Locate every malaria parasite and every leukocyte.
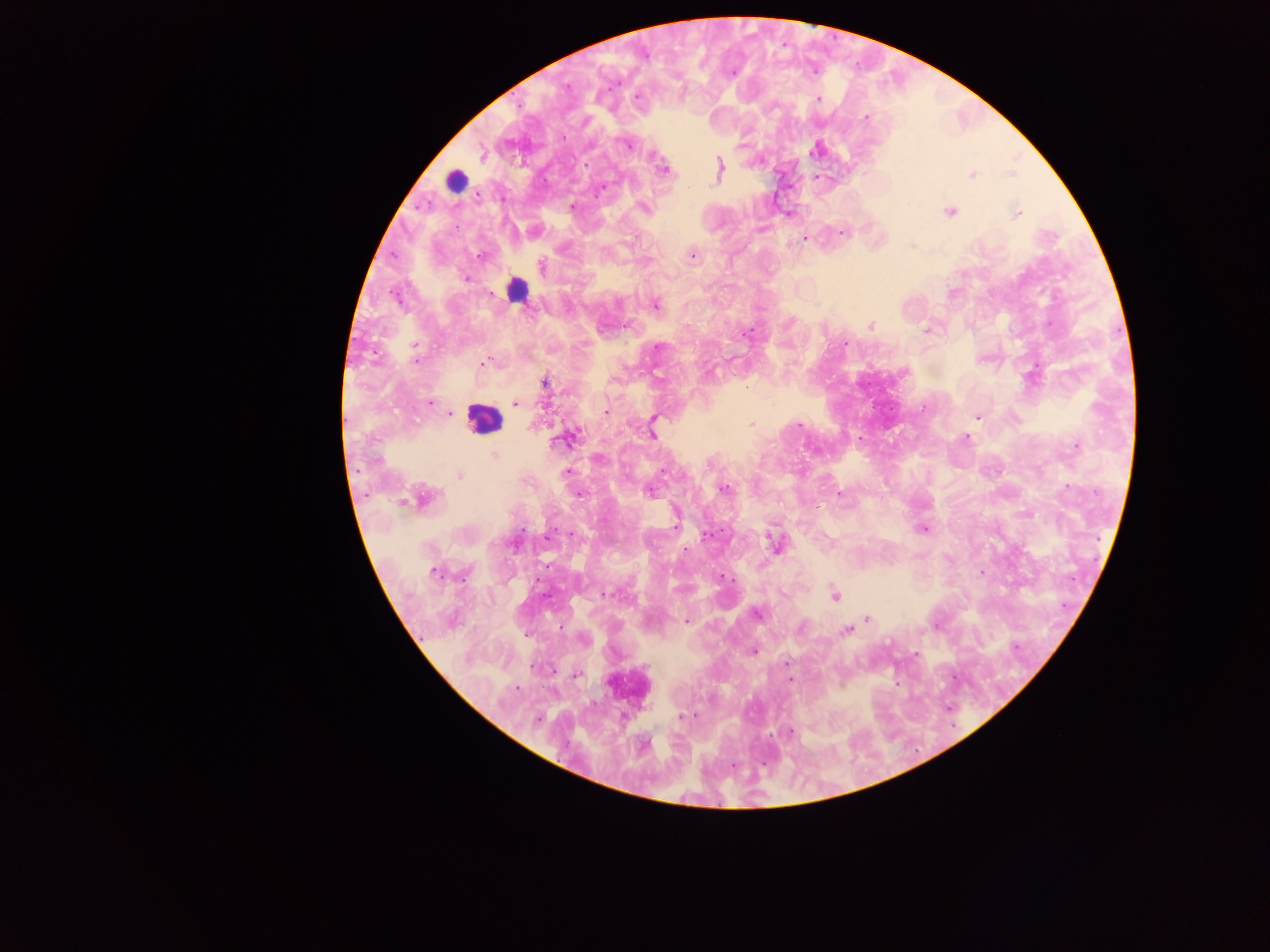

Approximate centers as x y in pixels.
Malaria parasites: 637 97; 818 99; 865 117; 628 144; 815 149; 482 156; 719 168; 663 170; 972 174; 571 207; 643 208; 950 212; 1017 214; 841 232; 805 239; 692 255; 480 256; 542 267; 466 278; 656 304; 871 325; 926 331; 746 334; 415 347; 658 347; 415 361; 483 363; 613 380; 545 383; 746 387; 430 403; 515 403; 605 412; 450 414; 978 416; 751 425; 798 426; 652 434; 966 438; 564 439; 1076 447; 494 454; 566 472; 460 476; 724 490; 649 491; 839 493; 579 494; 424 498; 676 523; 923 529; 522 530; 706 536; 774 543; 685 550; 981 572; 434 573; 722 577; 605 594; 835 595; 757 614; 868 618; 685 621; 801 627; 846 630; 753 651; 786 663; 578 674; 516 688; 682 716; 538 719; 790 731.
Leukocytes: 456 181; 518 286; 482 418; 623 681.

Collected in Ghana. Mobile-phone photograph taken through the microscope. Image is 1270×952 pixels. Thick blood smear. One field of view.